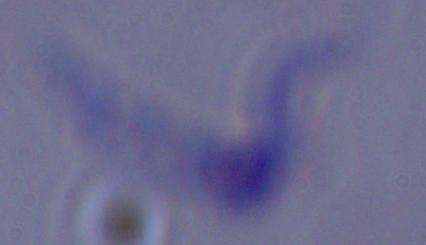

Captured at 1000x magnification. Micrograph. A trypanosome is shown.